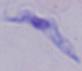

Summary:
  - Magnification: 1000x
  - Modality: micrograph
  - Identification: trypanosome